Give the extent of all Plasmodium vivax-infected red blood cells.
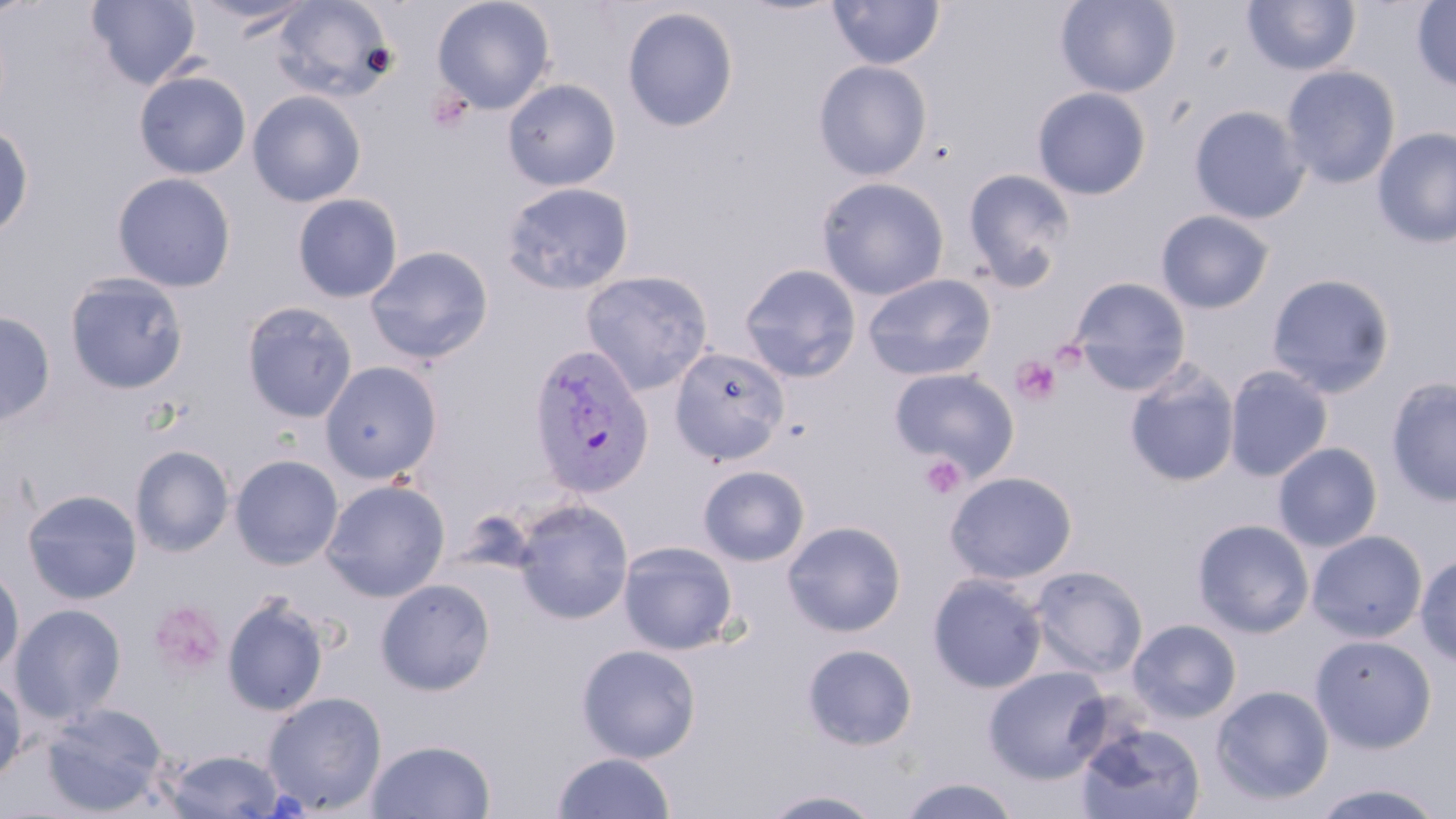

Approximate bounding boxes as (x1,y1)-(x2,y2) corner pairs in pixels.
Plasmodium vivax-infected red blood cells: (528,343)-(655,499).

Summary:
  - Platelet locations: (428,89)-(472,134), (1011,355)-(1063,406), (920,455)-(966,499), (149,600)-(226,678)
  - Uninfected red blood cell locations: (86,0)-(202,90), (190,0)-(318,34), (269,0)-(398,103), (432,0)-(555,115), (828,0)-(945,70), (1055,0)-(1181,98), (1240,0)-(1361,76), (1411,1)-(1456,92), (622,6)-(739,132), (812,60)-(932,180), (1281,65)-(1401,189), (134,70)-(251,179), (502,78)-(621,191), (1031,87)-(1151,200), (248,90)-(366,207), (1189,105)-(1310,224), (0,121)-(34,241), (1372,126)-(1456,248), (962,169)-(1074,291), (112,172)-(236,292), (816,176)-(950,300), (500,181)-(634,295), (292,193)-(403,303), (1155,209)-(1275,314), (365,245)-(494,365), (739,263)-(862,383), (580,270)-(714,395), (64,273)-(189,394), (862,273)-(996,381), (1266,273)-(1396,398), (1070,277)-(1192,395), (241,301)-(358,423), (0,311)-(56,426), (669,345)-(789,465), (319,360)-(443,484), (1124,361)-(1240,488), (1224,365)-(1334,481), (889,367)-(1019,478), (1385,377)-(1456,507), (1272,442)-(1383,552), (130,445)-(235,557), (229,455)-(343,570), (698,464)-(811,566), (944,471)-(1078,584), (321,479)-(450,601), (22,488)-(142,605), (512,498)-(633,624), (1192,518)-(1314,637), (782,520)-(907,637), (1306,530)-(1427,643), (617,540)-(739,655), (1415,554)-(1456,667), (0,564)-(25,676), (1030,565)-(1148,678), (927,573)-(1047,693), (376,578)-(496,696), (221,594)-(330,717), (10,603)-(127,725), (1128,618)-(1242,723), (1310,634)-(1437,753), (576,643)-(702,763), (802,643)-(918,751), (984,664)-(1112,784), (0,676)-(27,783), (1210,685)-(1334,805), (262,692)-(387,814), (41,703)-(168,815), (1074,720)-(1207,819), (366,738)-(496,819), (165,749)-(286,818), (552,752)-(675,818), (897,775)-(1020,818), (1309,782)-(1449,818), (758,788)-(887,818)
  - Slide-level diagnosis: Plasmodium vivax
  - Stain: May-Grünwald-Giemsa
  - Modality: optical microscopy
  - Magnification: 1000x
  - Image size: 1456×819 pixels
  - Preparation: thin blood film
  - Field of view: one of a larger specimen